Assess this cell for malaria.
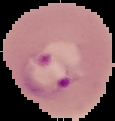
Parasitized.

preparation = thin blood film
image size = 115×121 pixels
image type = cell region segmented out of the field of view; surrounding area masked to black